Classify this cell by malaria status.
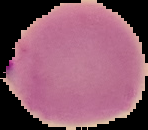

Parasitized.

Image is 148×130 pixels. The area outside the segmented cell region is set to black. From a thin blood film.